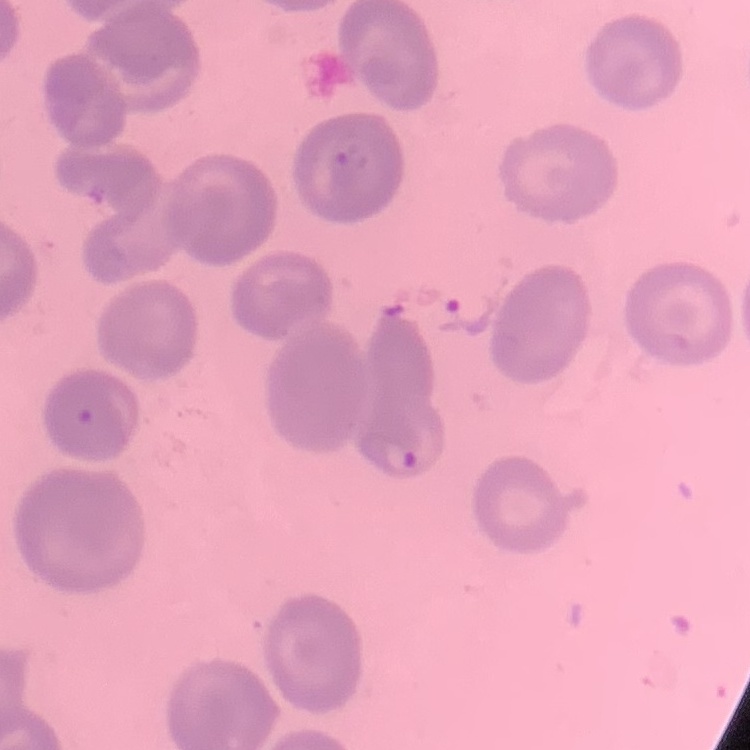

Summary:
  - Red blood cell morphology: no rouleaux formation
  - Stain: Field's or Giemsa
  - Preparation: thin blood smear
  - Image type: square crop of a larger photomicrograph